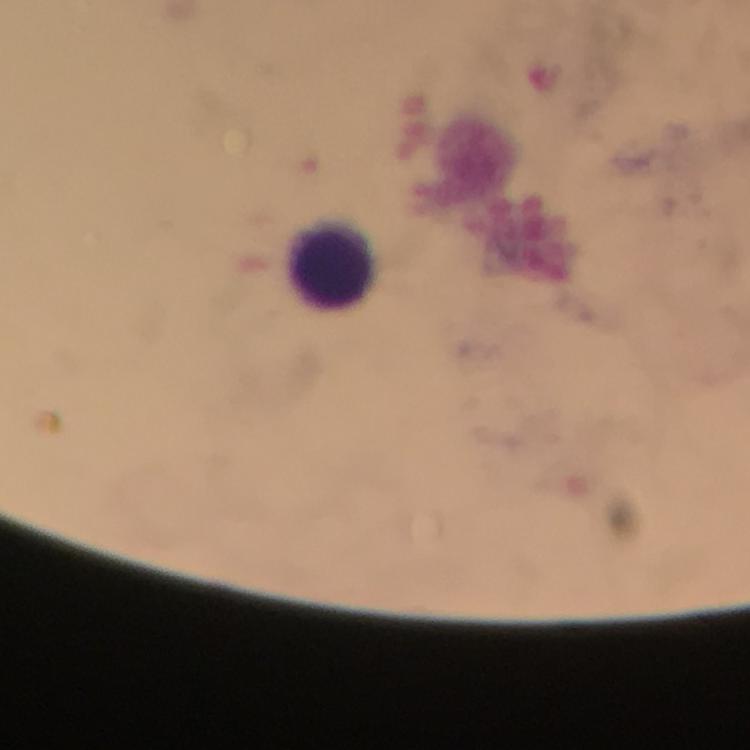 Approximate centers as {x, y} in pixels. Leukocyte locations: {332, 264}. Photographed with a smartphone mounted on the microscope. Immersion oil applied. Malaria parasites: none detected. 100x magnification. Giemsa-stained preparation. From a malaria diagnostic workup. Thick blood film. A crop from one field of view. Image is 750×750 pixels.